Outline each blood parasite and name the species.
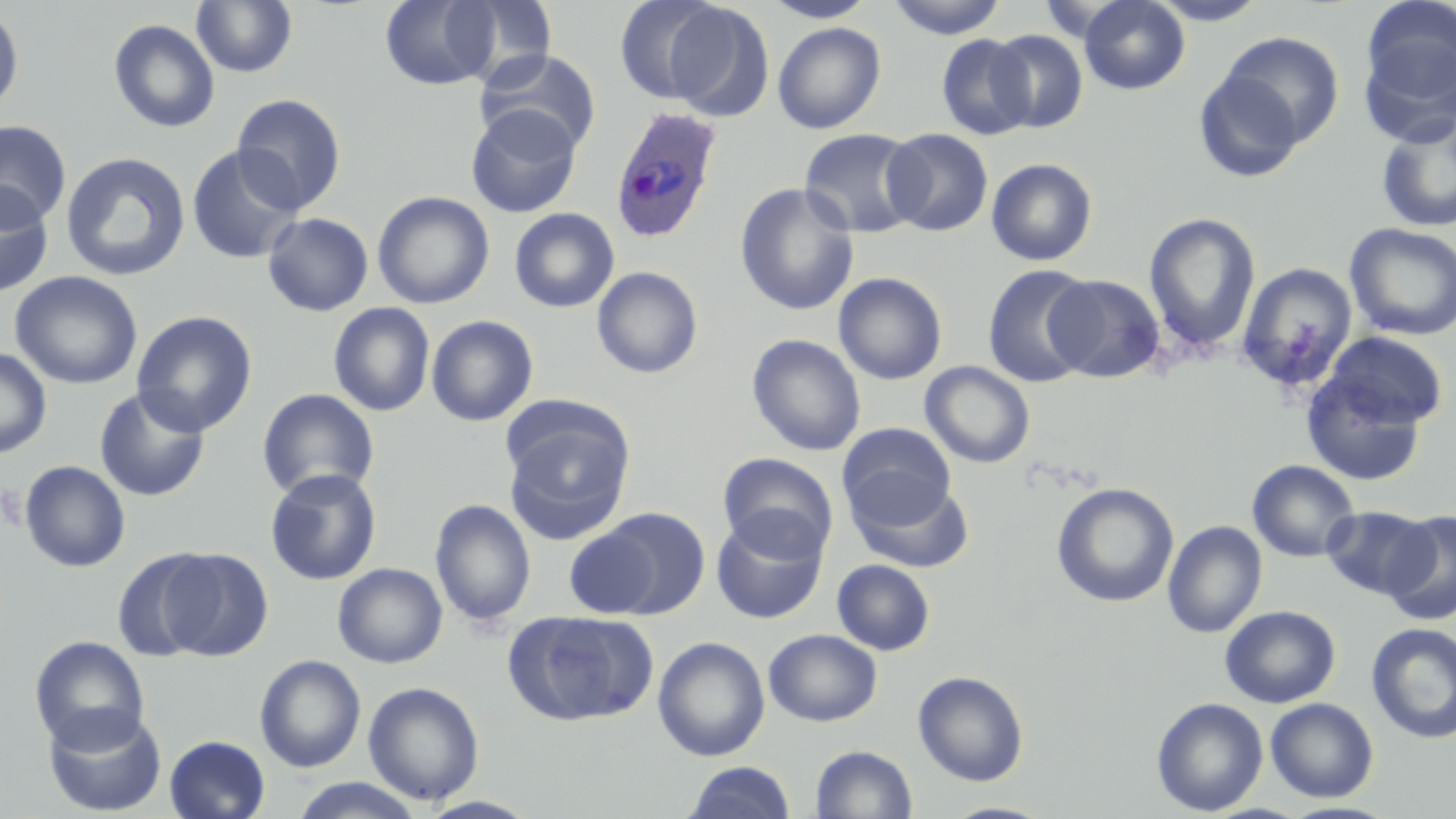

Approximate bounding boxes as [x1, y1, x2, y2] in pixels.
Plasmodium ovale-infected red blood cells: [609, 105, 724, 244].
No Plasmodium falciparum, Plasmodium malariae, Plasmodium vivax, Babesia divergens, or Trypanosoma brucei observed.

Uninfected red blood cell locations: [380, 0, 500, 90], [451, 0, 557, 86], [615, 0, 729, 105], [761, 0, 879, 22], [885, 0, 1008, 39], [1078, 0, 1191, 94], [1147, 0, 1269, 25], [191, 1, 298, 78], [662, 2, 775, 120], [1358, 4, 1456, 141], [0, 6, 24, 114], [108, 18, 220, 134], [773, 22, 886, 134], [988, 29, 1088, 133], [1218, 31, 1345, 148], [936, 33, 1037, 140], [474, 48, 601, 155], [1193, 69, 1307, 183], [231, 93, 347, 214], [466, 105, 582, 217], [1376, 116, 1456, 233], [0, 121, 72, 225], [798, 128, 923, 238], [881, 128, 993, 236], [186, 144, 304, 264], [60, 151, 191, 282], [986, 158, 1098, 266], [735, 183, 859, 316], [0, 184, 54, 298], [372, 191, 495, 309], [509, 208, 619, 312], [1143, 211, 1261, 359], [262, 212, 373, 316], [1345, 223, 1456, 341], [1237, 261, 1358, 392], [983, 265, 1097, 387], [592, 266, 703, 379], [10, 271, 143, 389], [833, 272, 947, 384], [1045, 273, 1165, 383], [329, 303, 435, 416], [132, 311, 258, 437], [427, 315, 538, 426], [1320, 330, 1448, 433], [747, 333, 866, 456], [0, 346, 52, 459], [920, 361, 1035, 468], [1300, 367, 1430, 487], [93, 386, 211, 502], [257, 388, 379, 500], [502, 413, 636, 544], [837, 423, 956, 527], [716, 452, 839, 560], [1247, 459, 1361, 562], [19, 460, 131, 572], [265, 468, 382, 585], [847, 476, 974, 574], [1052, 482, 1179, 608], [430, 498, 536, 627], [1322, 505, 1435, 600], [596, 507, 710, 617], [1383, 510, 1456, 626], [711, 512, 828, 623], [1163, 520, 1267, 638], [564, 525, 664, 618], [152, 547, 273, 660], [112, 548, 219, 662], [832, 559, 935, 655], [333, 563, 447, 668], [1219, 605, 1340, 707], [505, 609, 656, 726], [1366, 622, 1456, 743], [763, 629, 882, 726], [29, 635, 150, 752], [653, 636, 770, 761], [254, 654, 366, 773], [913, 670, 1028, 785], [363, 681, 485, 805], [1152, 697, 1268, 816], [1265, 697, 1378, 802], [42, 705, 167, 817], [163, 735, 271, 819], [810, 745, 918, 819], [682, 761, 797, 819], [289, 778, 425, 818], [940, 801, 1055, 819], [1280, 801, 1400, 819]. Platelet locations: [0, 482, 25, 532]. Slide-level diagnosis: Plasmodium ovale. Thin blood film. 1000x magnification. Image is 1456×819 pixels. Light microscopy. Single field of view. May-Grünwald-Giemsa stain.